Name the blood parasite species.
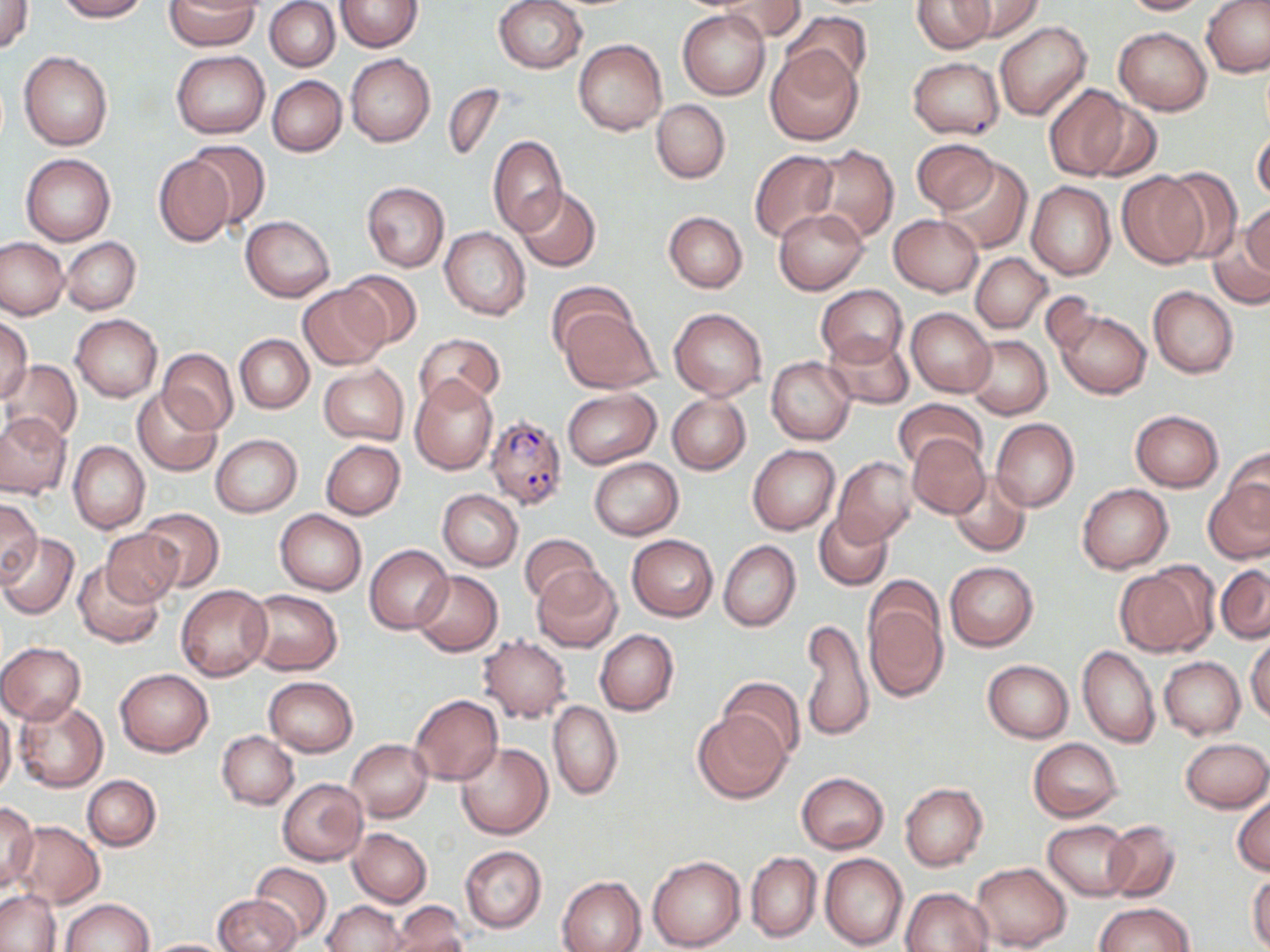

Plasmodium falciparum.

Approximate bounding boxes as named x1/y1/x2/y2 corners in pixels. Plasmodium falciparum-infected red blood cell locations: (x1=485, y1=412, x2=568, y2=510). Uninfected red blood cell locations: (x1=54, y1=0, x2=148, y2=21), (x1=164, y1=0, x2=259, y2=51), (x1=335, y1=0, x2=420, y2=52), (x1=494, y1=0, x2=586, y2=74), (x1=712, y1=0, x2=806, y2=43), (x1=912, y1=0, x2=994, y2=53), (x1=957, y1=0, x2=1043, y2=42), (x1=1117, y1=0, x2=1215, y2=16), (x1=1, y1=1, x2=33, y2=53), (x1=1202, y1=1, x2=1270, y2=78), (x1=266, y1=2, x2=340, y2=71), (x1=677, y1=9, x2=770, y2=99), (x1=782, y1=11, x2=872, y2=91), (x1=994, y1=20, x2=1092, y2=121), (x1=1114, y1=26, x2=1213, y2=115), (x1=574, y1=39, x2=667, y2=136), (x1=765, y1=46, x2=864, y2=144), (x1=19, y1=50, x2=114, y2=151), (x1=171, y1=50, x2=269, y2=138), (x1=345, y1=54, x2=435, y2=147), (x1=907, y1=56, x2=1005, y2=139), (x1=267, y1=76, x2=346, y2=156), (x1=443, y1=84, x2=505, y2=162), (x1=1042, y1=84, x2=1134, y2=181), (x1=1076, y1=94, x2=1162, y2=182), (x1=652, y1=98, x2=730, y2=184), (x1=1252, y1=128, x2=1270, y2=204), (x1=488, y1=137, x2=568, y2=236), (x1=912, y1=138, x2=999, y2=214), (x1=182, y1=141, x2=271, y2=229), (x1=806, y1=145, x2=899, y2=244), (x1=750, y1=149, x2=841, y2=245), (x1=20, y1=153, x2=116, y2=246), (x1=153, y1=154, x2=236, y2=246), (x1=937, y1=157, x2=1032, y2=254), (x1=1160, y1=168, x2=1243, y2=262), (x1=1117, y1=171, x2=1208, y2=267), (x1=1025, y1=180, x2=1116, y2=280), (x1=362, y1=182, x2=449, y2=271), (x1=515, y1=186, x2=601, y2=272), (x1=1241, y1=202, x2=1270, y2=285), (x1=774, y1=208, x2=869, y2=294), (x1=664, y1=211, x2=747, y2=293), (x1=889, y1=213, x2=983, y2=295), (x1=1213, y1=213, x2=1270, y2=307), (x1=241, y1=215, x2=335, y2=301), (x1=440, y1=228, x2=530, y2=320), (x1=0, y1=237, x2=70, y2=320), (x1=62, y1=238, x2=140, y2=314), (x1=971, y1=252, x2=1051, y2=333), (x1=336, y1=270, x2=423, y2=348), (x1=545, y1=283, x2=637, y2=360), (x1=297, y1=284, x2=393, y2=369), (x1=816, y1=284, x2=908, y2=369), (x1=1148, y1=286, x2=1238, y2=378), (x1=557, y1=306, x2=660, y2=394), (x1=669, y1=307, x2=767, y2=400), (x1=906, y1=307, x2=996, y2=397), (x1=1052, y1=307, x2=1151, y2=398), (x1=71, y1=313, x2=163, y2=402), (x1=0, y1=314, x2=33, y2=405), (x1=416, y1=332, x2=503, y2=408), (x1=236, y1=335, x2=313, y2=412), (x1=823, y1=335, x2=914, y2=410), (x1=964, y1=336, x2=1051, y2=419), (x1=157, y1=349, x2=238, y2=434), (x1=1, y1=358, x2=82, y2=447), (x1=767, y1=358, x2=856, y2=444), (x1=318, y1=363, x2=409, y2=447), (x1=410, y1=375, x2=498, y2=475), (x1=562, y1=388, x2=661, y2=468), (x1=132, y1=389, x2=222, y2=475), (x1=667, y1=394, x2=751, y2=474), (x1=893, y1=398, x2=987, y2=473), (x1=1130, y1=409, x2=1224, y2=492), (x1=0, y1=412, x2=70, y2=498), (x1=991, y1=418, x2=1079, y2=511), (x1=212, y1=434, x2=301, y2=516), (x1=907, y1=434, x2=989, y2=519), (x1=321, y1=439, x2=405, y2=519), (x1=68, y1=441, x2=149, y2=535), (x1=748, y1=445, x2=839, y2=534), (x1=1223, y1=445, x2=1270, y2=527), (x1=833, y1=457, x2=919, y2=547), (x1=589, y1=458, x2=683, y2=540), (x1=947, y1=473, x2=1031, y2=556), (x1=1205, y1=479, x2=1270, y2=565), (x1=1076, y1=484, x2=1173, y2=573), (x1=437, y1=489, x2=523, y2=571), (x1=0, y1=498, x2=42, y2=586), (x1=140, y1=507, x2=224, y2=590), (x1=275, y1=509, x2=367, y2=595), (x1=815, y1=509, x2=893, y2=590), (x1=101, y1=528, x2=186, y2=606), (x1=0, y1=533, x2=79, y2=619), (x1=517, y1=533, x2=602, y2=607), (x1=627, y1=534, x2=718, y2=620), (x1=718, y1=541, x2=800, y2=632), (x1=365, y1=546, x2=453, y2=635), (x1=74, y1=561, x2=165, y2=648), (x1=946, y1=561, x2=1037, y2=652), (x1=1114, y1=563, x2=1218, y2=657), (x1=532, y1=564, x2=624, y2=653), (x1=1215, y1=564, x2=1270, y2=643), (x1=412, y1=571, x2=502, y2=657), (x1=175, y1=584, x2=273, y2=679), (x1=861, y1=585, x2=949, y2=703), (x1=244, y1=589, x2=342, y2=676), (x1=800, y1=619, x2=875, y2=744), (x1=595, y1=629, x2=678, y2=716), (x1=477, y1=634, x2=572, y2=722), (x1=1246, y1=636, x2=1270, y2=723), (x1=0, y1=643, x2=86, y2=724), (x1=1078, y1=645, x2=1160, y2=748), (x1=1159, y1=656, x2=1245, y2=739), (x1=982, y1=659, x2=1073, y2=741), (x1=115, y1=668, x2=212, y2=756), (x1=264, y1=676, x2=358, y2=756), (x1=721, y1=677, x2=805, y2=761), (x1=408, y1=693, x2=503, y2=786), (x1=15, y1=698, x2=108, y2=791), (x1=547, y1=699, x2=622, y2=800), (x1=0, y1=706, x2=17, y2=798), (x1=692, y1=710, x2=788, y2=803), (x1=217, y1=731, x2=299, y2=809), (x1=1181, y1=737, x2=1270, y2=813), (x1=1028, y1=738, x2=1122, y2=820), (x1=345, y1=740, x2=431, y2=822), (x1=455, y1=742, x2=553, y2=839), (x1=796, y1=772, x2=888, y2=853), (x1=83, y1=776, x2=161, y2=850), (x1=277, y1=778, x2=368, y2=865), (x1=899, y1=782, x2=989, y2=871), (x1=1232, y1=791, x2=1270, y2=877), (x1=0, y1=800, x2=39, y2=890), (x1=1043, y1=820, x2=1137, y2=900), (x1=1102, y1=820, x2=1181, y2=902), (x1=11, y1=821, x2=104, y2=908), (x1=348, y1=828, x2=432, y2=907), (x1=460, y1=846, x2=547, y2=932), (x1=746, y1=852, x2=821, y2=942), (x1=820, y1=853, x2=907, y2=950), (x1=647, y1=855, x2=744, y2=950), (x1=251, y1=862, x2=332, y2=943), (x1=972, y1=862, x2=1070, y2=950), (x1=1247, y1=871, x2=1270, y2=952), (x1=557, y1=876, x2=647, y2=952), (x1=902, y1=888, x2=993, y2=952), (x1=0, y1=890, x2=60, y2=951), (x1=213, y1=894, x2=300, y2=952), (x1=59, y1=899, x2=153, y2=952), (x1=323, y1=900, x2=406, y2=951), (x1=387, y1=901, x2=469, y2=952), (x1=1093, y1=903, x2=1194, y2=952), (x1=141, y1=938, x2=234, y2=951). Image is 1270×952 pixels. 1000x magnification. Single field of view. Thin blood smear. Optical microscopy. May-Grünwald-Giemsa stain.